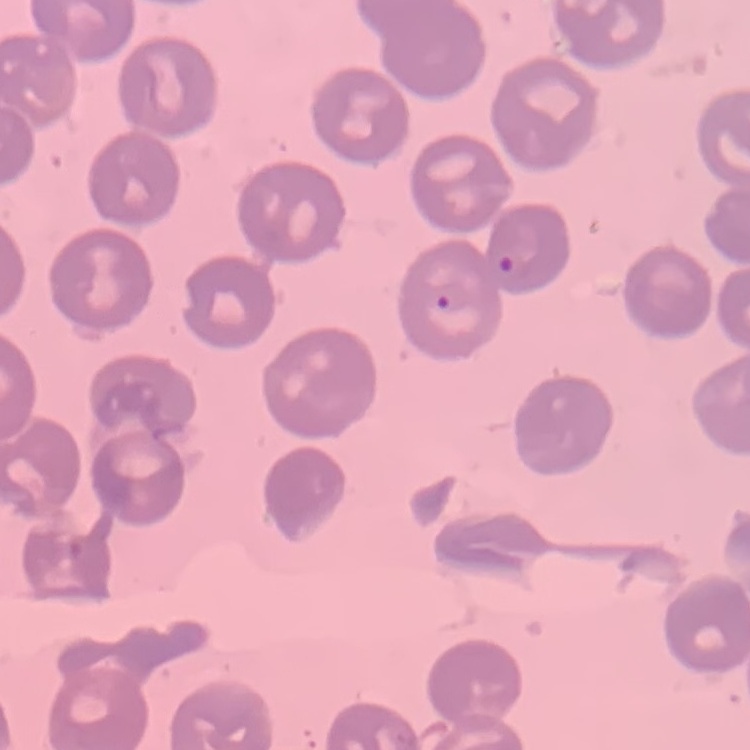
{
  "red_blood_cell_morphology": "no rouleaux formation",
  "stain": "Field's or Giemsa",
  "image_type": "square crop of a larger photomicrograph",
  "preparation": "thin blood smear"
}